Report the malaria status of this cell.
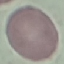

Uninfected.

Summary:
  - Stain: Giemsa
  - Preparation: thin smear
  - Image type: cell patch, automatically extracted from a larger field of view and resized to 64 × 64 pixels
  - Capture: smartphone camera at the microscope eyepiece